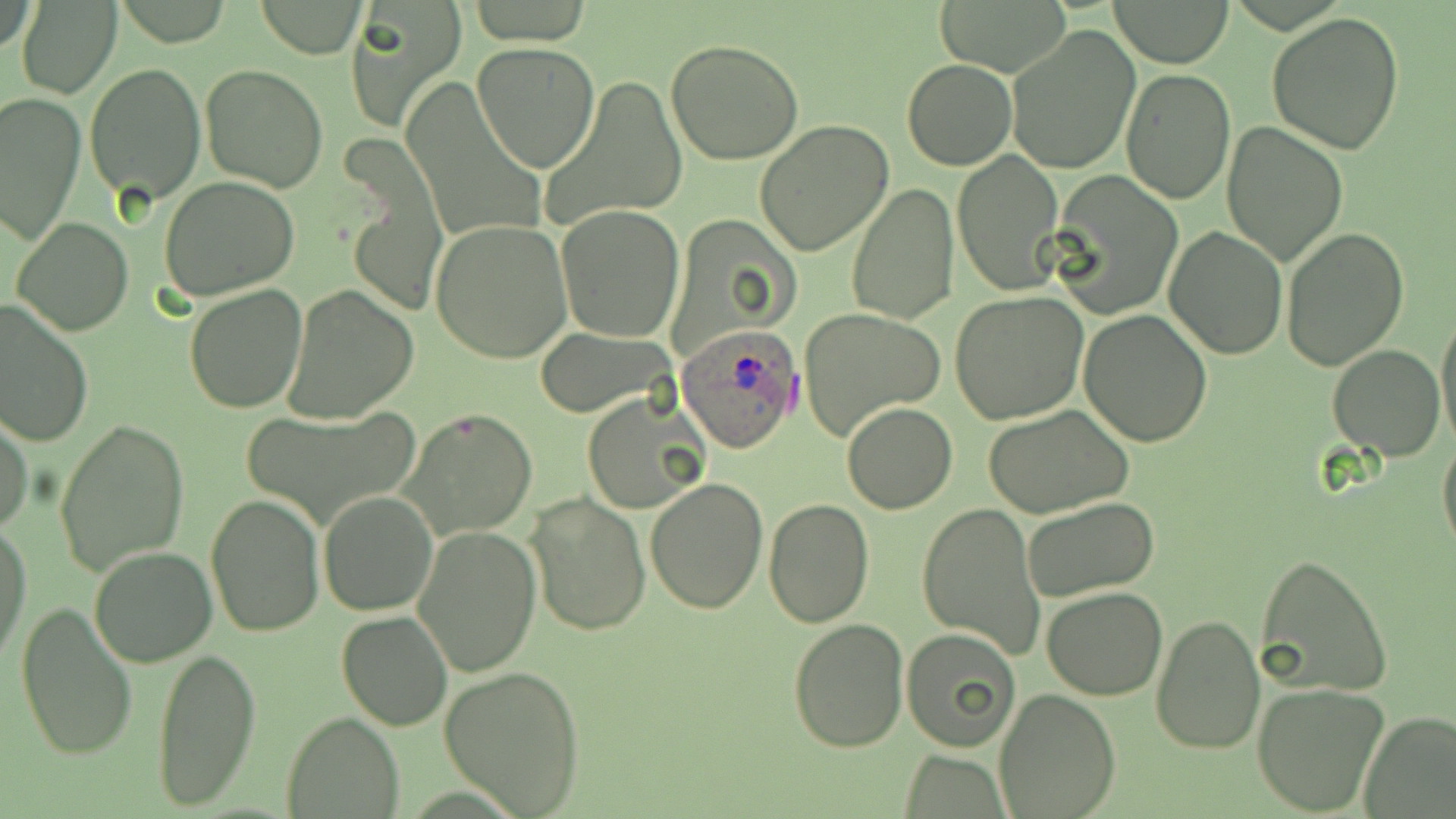

Summary:
  - Coordinate format: approximate bounding boxes as (x1, y1, x2, y2) in pixels
  - Plasmodium ovale-infected red blood cell locations: (676, 327, 801, 452)
  - Uninfected red blood cell locations: (1111, 0, 1233, 68), (17, 1, 122, 99), (346, 1, 466, 128), (934, 1, 1068, 75), (254, 2, 367, 56), (1265, 13, 1406, 155), (1005, 25, 1140, 176), (664, 39, 806, 167), (472, 42, 600, 172), (902, 59, 1016, 170), (84, 63, 207, 205), (200, 64, 328, 192), (1119, 67, 1234, 204), (546, 75, 688, 227), (404, 81, 548, 246), (2, 92, 85, 244), (754, 120, 894, 257), (1220, 120, 1349, 266), (952, 149, 1064, 296), (341, 153, 449, 319), (1048, 173, 1181, 321), (158, 177, 300, 301), (846, 183, 959, 323), (554, 203, 685, 342), (11, 217, 132, 336), (431, 218, 573, 363), (1164, 226, 1289, 359), (1282, 227, 1409, 371), (184, 284, 308, 412), (280, 285, 419, 422), (950, 291, 1089, 424), (0, 301, 94, 447), (1435, 306, 1456, 450), (1078, 308, 1212, 447), (798, 310, 947, 439), (531, 328, 677, 418), (1327, 345, 1446, 460), (584, 394, 708, 516), (841, 401, 959, 515), (983, 404, 1134, 518), (238, 406, 423, 528), (399, 408, 538, 542), (0, 412, 32, 535), (55, 418, 189, 578), (1437, 433, 1456, 561), (643, 477, 768, 614), (525, 491, 651, 636), (318, 492, 437, 616), (206, 493, 326, 636), (1020, 497, 1160, 604), (764, 498, 874, 628), (916, 502, 1045, 659), (0, 521, 32, 667), (413, 524, 542, 678), (89, 544, 218, 666), (1257, 555, 1393, 699), (1042, 585, 1168, 699), (15, 597, 139, 763), (337, 611, 452, 729), (1152, 614, 1265, 756), (788, 619, 909, 754), (902, 628, 1020, 750), (150, 646, 260, 810), (439, 667, 587, 815), (1251, 683, 1390, 815), (995, 690, 1120, 817), (1359, 709, 1456, 818), (283, 711, 401, 818), (899, 749, 1007, 817)
  - Slide-level diagnosis: Plasmodium ovale
  - Stain: May-Grünwald-Giemsa
  - Preparation: thin blood film
  - Image size: 1456×819 pixels
  - Modality: light microscopy
  - Field of view: single
  - Magnification: 1000x